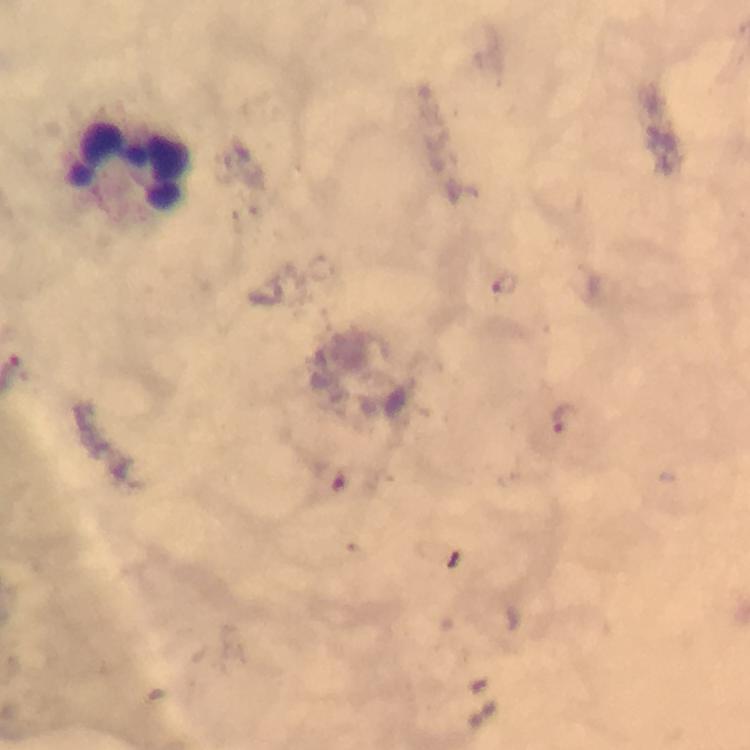

stain = Giemsa
image size = 750×750 pixels
malaria parasite locations = approximate centers as {x, y} in pixels: {505, 285}, {564, 420}
cropped from = one field of view
magnification = 100x
context = from a diagnostic examination for malaria
immersion oil = applied
capture = smartphone mounted on the microscope
leukocyte locations = approximate centers as {x, y} in pixels: {130, 166}
preparation = thick blood smear